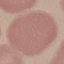

Summary:
  - Malaria status: uninfected
  - Capture: smartphone camera at the microscope eyepiece
  - Stain: Giemsa
  - Preparation: thin blood film
  - Image type: automatically extracted cell patch, resized to 64 × 64 pixels